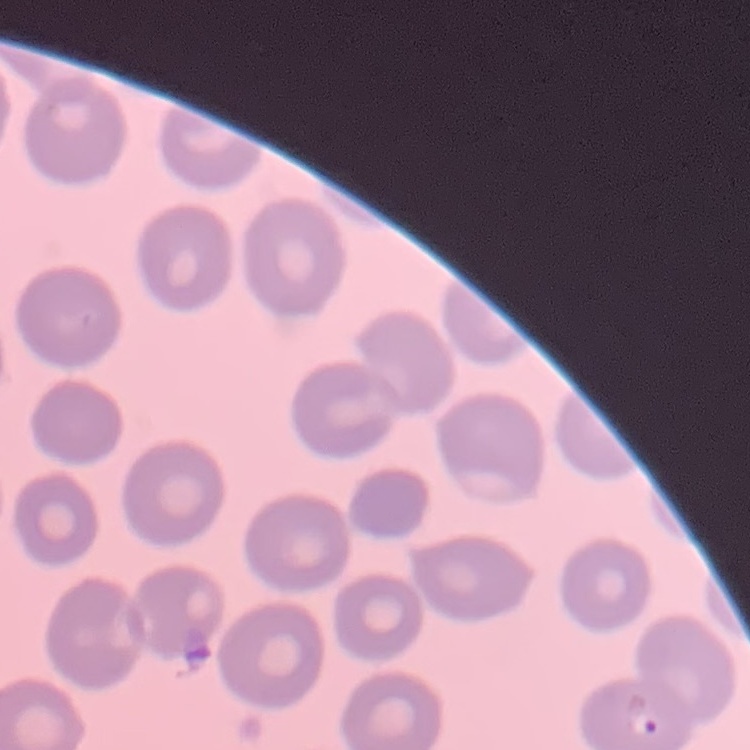

The erythrocytes exhibit no rouleaux formation. Square crop of a larger photomicrograph. Thin blood smear. Field's or Giemsa stain.